Comment on the morphology of the red blood cells.
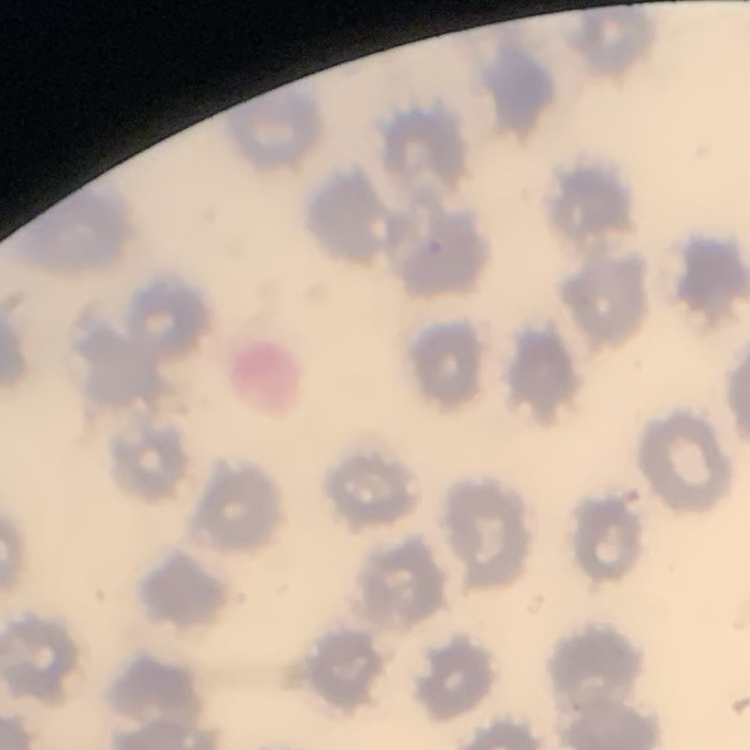

They show no rouleaux formation.

preparation = thin blood smear
image type = square crop of a larger photomicrograph
stain = Field's or Giemsa